Identify the cell.
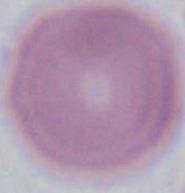
An erythrocyte.

Photomicrograph. 1000x magnification.